Locate every uninfected red blood cell.
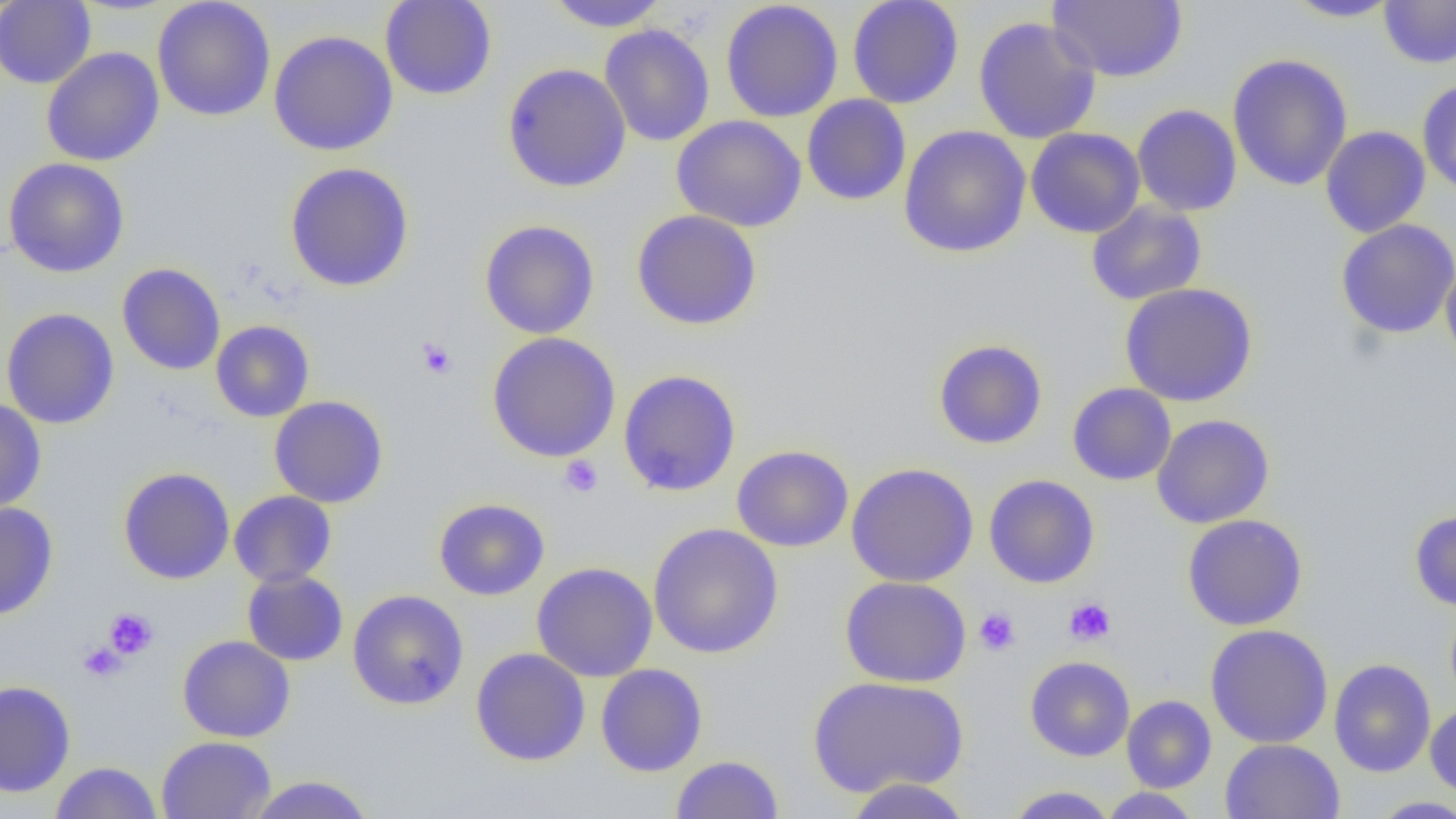

Approximate bounding boxes as [x1, y1, x2, y2] in pixels.
Uninfected red blood cells: [380, 0, 497, 100], [543, 0, 671, 31], [847, 0, 965, 109], [1047, 0, 1187, 82], [1283, 0, 1404, 22], [0, 1, 96, 88], [152, 1, 276, 122], [720, 1, 843, 123], [1379, 1, 1456, 69], [973, 16, 1102, 144], [599, 24, 715, 147], [268, 30, 398, 156], [41, 47, 165, 167], [1227, 53, 1353, 191], [502, 63, 632, 192], [1417, 79, 1456, 198], [802, 94, 911, 206], [1131, 104, 1242, 216], [671, 115, 807, 232], [898, 124, 1032, 258], [1320, 126, 1431, 238], [1025, 127, 1146, 238], [3, 158, 130, 278], [284, 162, 415, 292], [1086, 200, 1207, 306], [631, 210, 763, 331], [1336, 219, 1456, 338], [479, 220, 600, 339], [1440, 259, 1456, 368], [117, 263, 226, 375], [1119, 283, 1258, 407], [2, 308, 119, 430], [211, 320, 314, 422], [486, 332, 621, 462], [933, 339, 1048, 450], [618, 369, 742, 496], [1067, 382, 1177, 485], [268, 395, 389, 508], [0, 397, 46, 514], [1151, 414, 1275, 529], [731, 444, 854, 552], [846, 462, 979, 587], [118, 467, 235, 585], [984, 474, 1100, 589], [229, 491, 337, 588], [433, 497, 550, 601], [0, 501, 58, 621], [1409, 509, 1456, 612], [1182, 514, 1308, 631], [647, 523, 784, 659], [531, 561, 658, 682], [241, 569, 349, 666], [840, 576, 972, 688], [347, 589, 469, 710], [1445, 602, 1456, 712], [1205, 624, 1334, 748], [177, 635, 295, 742], [470, 648, 590, 766], [1024, 656, 1136, 761], [1329, 659, 1436, 777], [595, 663, 708, 777], [807, 676, 969, 797], [0, 680, 76, 797], [1121, 695, 1217, 793], [1424, 701, 1456, 799], [156, 736, 275, 818], [1220, 738, 1345, 819], [670, 754, 784, 818], [50, 761, 162, 819], [245, 775, 376, 819], [843, 777, 973, 819], [1004, 786, 1118, 818], [1098, 787, 1203, 818], [1368, 796, 1456, 818].

Platelet locations: [416, 337, 457, 379], [559, 455, 604, 497], [1064, 597, 1116, 646], [103, 607, 158, 659], [974, 607, 1020, 656], [78, 641, 126, 683]. Slide-level diagnosis: no evidence of blood parasites. 1000x magnification. Optical microscopy. Image is 1456×819 pixels. One field of a larger specimen. Thin blood smear.